Identify the parasite.
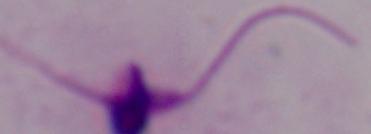

Leishmania.

Photomicrograph. Captured at 1000x magnification.